Classify this cell by malaria status.
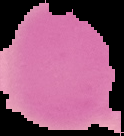
Uninfected.

image_size: 124×136 pixels
image_type: cell region segmented out of the field of view; surrounding area masked to black
preparation: thin blood smear